Give a bounding box for every Plasmodium parasite.
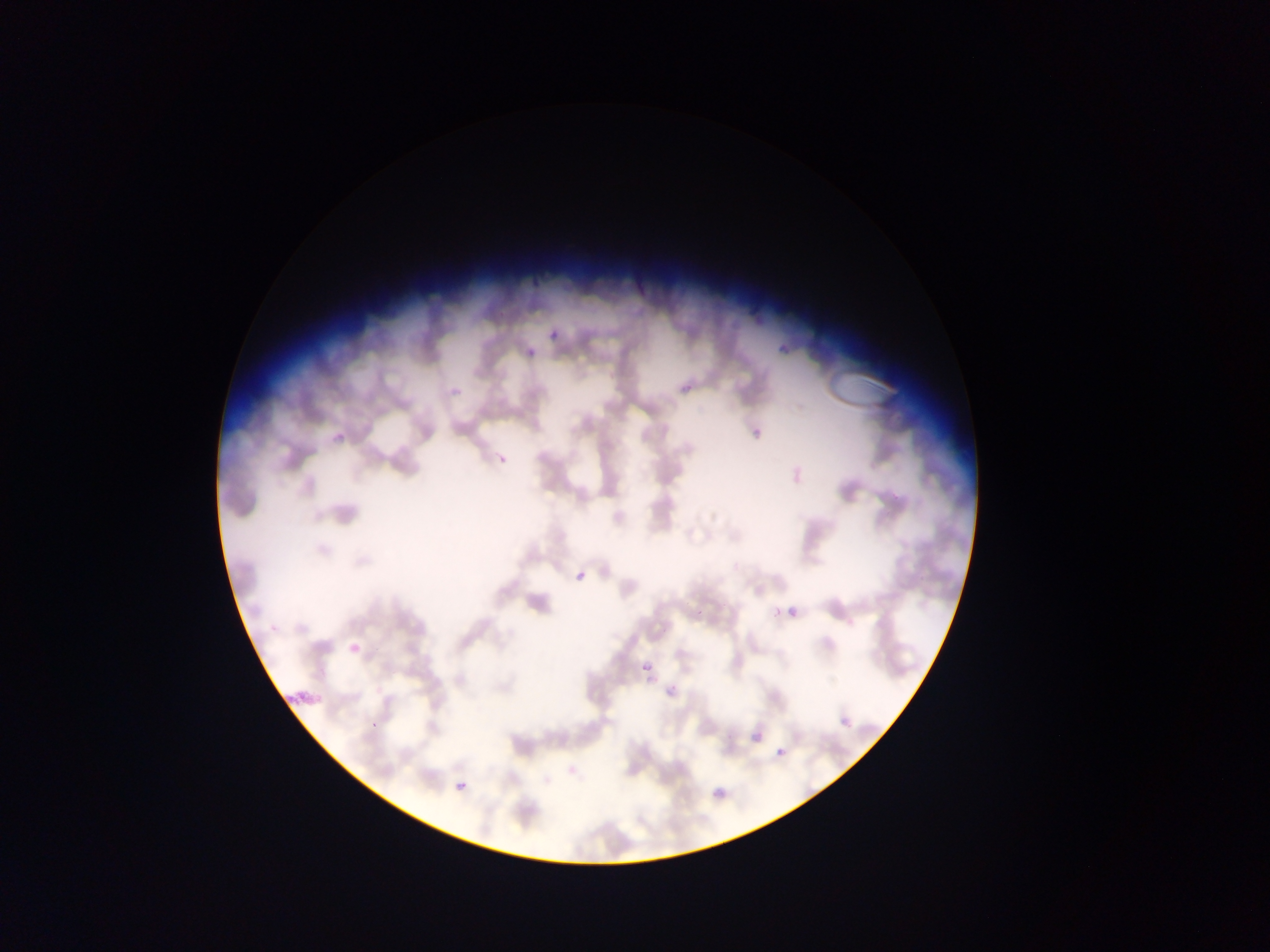

Approximate bounding boxes as left top right bottom in pixels.
Plasmodium parasites: 550 330 560 340; 519 349 535 360; 445 378 469 397; 748 428 769 443; 496 455 507 464; 576 571 585 580; 773 608 782 618; 788 608 798 617; 345 641 362 660; 643 663 650 671; 658 681 684 700; 840 718 853 729; 753 731 762 740; 777 746 785 757; 568 766 577 774; 456 782 466 791.

capture = mobile-phone photograph through a microscope
preparation = thin blood smear
country = Ghana
image size = 1270×952 pixels
field of view = single